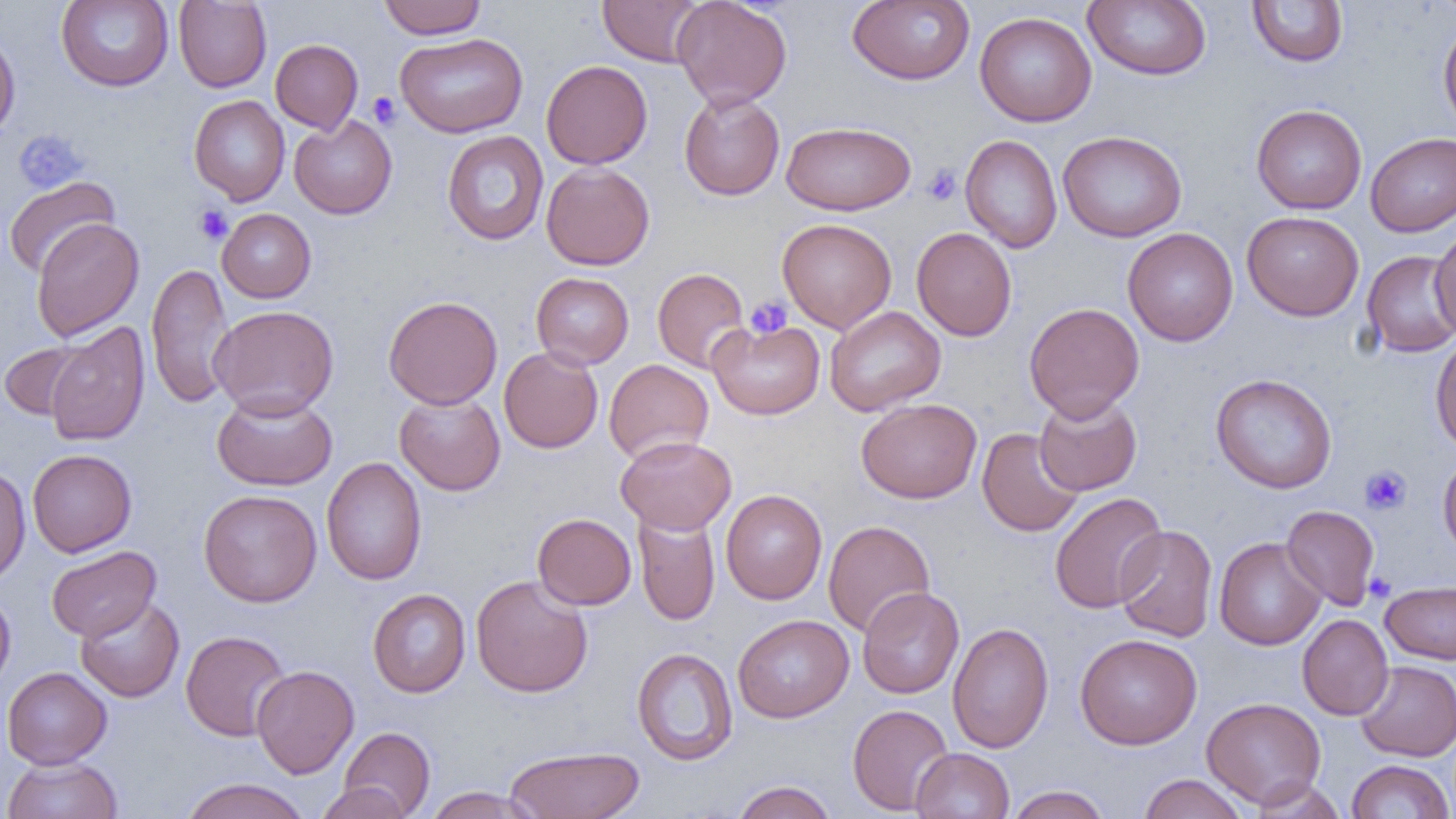 Approximate bounding boxes as (x1, y1, x2, y2) in pixels. Uninfected red blood cell locations: (56, 0, 174, 91), (379, 0, 486, 39), (597, 0, 706, 66), (671, 0, 793, 109), (847, 0, 975, 85), (1082, 0, 1212, 81), (173, 1, 271, 92), (1246, 1, 1349, 67), (974, 11, 1096, 126), (1438, 17, 1456, 137), (0, 28, 21, 142), (394, 32, 528, 138), (270, 39, 363, 134), (541, 60, 652, 169), (679, 90, 785, 201), (189, 95, 290, 206), (1251, 104, 1367, 214), (289, 114, 397, 219), (781, 121, 916, 215), (1058, 130, 1187, 242), (442, 131, 549, 245), (1365, 132, 1456, 237), (960, 134, 1063, 253), (541, 162, 655, 270), (3, 175, 120, 279), (217, 208, 316, 303), (1241, 211, 1364, 321), (30, 217, 144, 341), (777, 218, 897, 333), (1430, 223, 1456, 340), (911, 227, 1017, 341), (1122, 227, 1238, 346), (1361, 250, 1456, 358), (146, 262, 234, 410), (652, 268, 750, 373), (531, 272, 634, 369), (383, 295, 502, 410), (1024, 302, 1144, 422), (208, 304, 339, 419), (825, 306, 946, 416), (707, 318, 825, 419), (43, 322, 150, 447), (1430, 332, 1456, 453), (0, 341, 89, 420), (498, 347, 604, 453), (604, 359, 714, 464), (1210, 373, 1337, 494), (211, 391, 337, 491), (394, 392, 506, 496), (1034, 393, 1142, 496), (856, 398, 982, 503), (977, 427, 1084, 537), (615, 434, 737, 534), (27, 449, 137, 557), (1438, 454, 1456, 562), (321, 456, 427, 586), (0, 466, 30, 585), (198, 489, 322, 607), (721, 489, 827, 604), (1049, 492, 1168, 613), (1281, 505, 1380, 611), (633, 510, 720, 626), (532, 513, 636, 609), (823, 520, 935, 637), (1114, 525, 1217, 642), (1214, 537, 1326, 650), (46, 545, 161, 642), (471, 574, 593, 697), (1381, 580, 1456, 664), (857, 586, 964, 699), (0, 588, 16, 692), (367, 589, 470, 697), (75, 595, 184, 703), (732, 614, 854, 723), (1297, 614, 1393, 720), (947, 622, 1054, 753), (180, 630, 290, 741), (1075, 633, 1202, 750), (632, 647, 738, 766), (1355, 660, 1456, 761), (251, 665, 359, 779), (2, 666, 112, 769), (1201, 696, 1326, 808), (847, 704, 954, 815), (338, 727, 435, 817), (504, 745, 645, 819), (910, 747, 1015, 818), (1, 756, 123, 819), (1345, 760, 1455, 819), (1137, 773, 1250, 819), (179, 778, 310, 819), (1246, 778, 1346, 819), (730, 780, 838, 819), (314, 782, 414, 819), (1005, 785, 1112, 818), (423, 786, 541, 819). Platelet locations: (367, 92, 401, 128), (13, 129, 89, 194), (922, 164, 962, 205), (194, 205, 233, 245), (745, 296, 792, 340), (1360, 465, 1411, 515), (1365, 572, 1396, 602). Slide-level diagnosis: no evidence of blood parasites. Light microscopy. Single field of view. Captured at 1000x magnification. Thin blood film. Image is 1456×819 pixels.